Name the parasite shown.
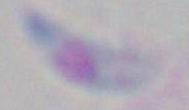
This is Toxoplasma gondii.

1000x magnification. Micrograph.